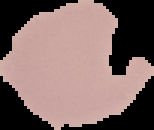

Summary:
  - Preparation: thin blood smear
  - Image size: 154×130 pixels
  - Image type: segmented cell region on a black background
  - Result: no Plasmodium parasites seen